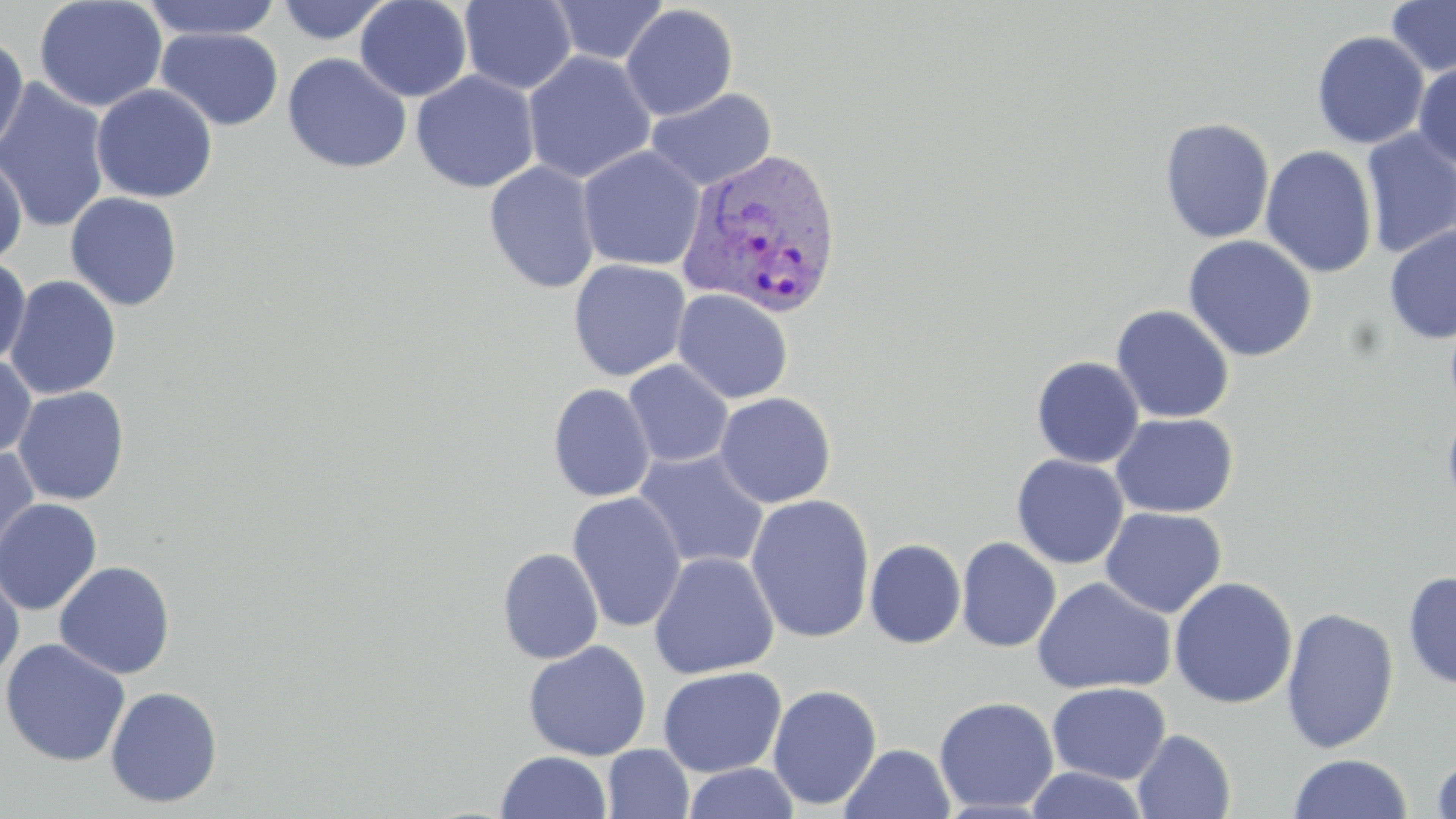

{
  "slide_level_diagnosis": "Plasmodium vivax",
  "magnification": "1000x",
  "uninfected_red_blood_cell_locations": "approximate bounding boxes as named x1/y1/x2/y2 corners in pixels: (x1=33, y1=0, x2=168, y2=113), (x1=138, y1=0, x2=285, y2=41), (x1=354, y1=0, x2=473, y2=102), (x1=1386, y1=0, x2=1456, y2=78), (x1=275, y1=1, x2=395, y2=44), (x1=458, y1=1, x2=577, y2=94), (x1=548, y1=1, x2=669, y2=65), (x1=620, y1=4, x2=739, y2=121), (x1=155, y1=27, x2=284, y2=131), (x1=1311, y1=30, x2=1429, y2=150), (x1=0, y1=34, x2=29, y2=159), (x1=522, y1=50, x2=657, y2=184), (x1=282, y1=52, x2=412, y2=174), (x1=1413, y1=62, x2=1456, y2=169), (x1=410, y1=70, x2=540, y2=193), (x1=0, y1=78, x2=111, y2=234), (x1=91, y1=83, x2=218, y2=203), (x1=644, y1=87, x2=777, y2=191), (x1=1158, y1=117, x2=1275, y2=244), (x1=1361, y1=128, x2=1456, y2=260), (x1=1260, y1=145, x2=1378, y2=278), (x1=577, y1=146, x2=704, y2=271), (x1=0, y1=151, x2=27, y2=269), (x1=483, y1=160, x2=601, y2=295), (x1=65, y1=191, x2=184, y2=311), (x1=1384, y1=225, x2=1456, y2=344), (x1=1182, y1=235, x2=1318, y2=362), (x1=0, y1=257, x2=31, y2=367), (x1=568, y1=259, x2=691, y2=381), (x1=4, y1=275, x2=121, y2=400), (x1=673, y1=288, x2=794, y2=404), (x1=1444, y1=302, x2=1456, y2=420), (x1=1110, y1=305, x2=1235, y2=424), (x1=0, y1=355, x2=37, y2=461), (x1=1030, y1=356, x2=1145, y2=468), (x1=622, y1=360, x2=734, y2=468), (x1=547, y1=383, x2=656, y2=503), (x1=12, y1=386, x2=130, y2=506), (x1=715, y1=391, x2=837, y2=508), (x1=1442, y1=403, x2=1456, y2=518), (x1=1110, y1=412, x2=1238, y2=518), (x1=0, y1=446, x2=40, y2=573), (x1=633, y1=448, x2=770, y2=571), (x1=1011, y1=454, x2=1129, y2=569), (x1=567, y1=491, x2=687, y2=633), (x1=745, y1=494, x2=876, y2=644), (x1=0, y1=497, x2=103, y2=615), (x1=1100, y1=506, x2=1227, y2=619), (x1=956, y1=537, x2=1061, y2=652), (x1=864, y1=538, x2=967, y2=649), (x1=497, y1=547, x2=604, y2=665), (x1=648, y1=551, x2=780, y2=679), (x1=54, y1=561, x2=176, y2=680), (x1=0, y1=564, x2=25, y2=680), (x1=1402, y1=570, x2=1456, y2=690), (x1=1167, y1=576, x2=1298, y2=709), (x1=1032, y1=577, x2=1177, y2=695), (x1=1280, y1=606, x2=1399, y2=753), (x1=0, y1=638, x2=131, y2=766), (x1=523, y1=641, x2=651, y2=761), (x1=657, y1=666, x2=788, y2=777), (x1=1047, y1=682, x2=1171, y2=784), (x1=767, y1=683, x2=882, y2=811), (x1=105, y1=685, x2=223, y2=808), (x1=934, y1=696, x2=1059, y2=814), (x1=1133, y1=729, x2=1236, y2=819), (x1=839, y1=743, x2=955, y2=819), (x1=603, y1=745, x2=694, y2=819), (x1=495, y1=750, x2=612, y2=819), (x1=1430, y1=751, x2=1456, y2=818), (x1=1288, y1=753, x2=1414, y2=818), (x1=682, y1=762, x2=801, y2=819), (x1=1024, y1=767, x2=1149, y2=819)",
  "image_size": "1456×819 pixels",
  "stain": "May-Grünwald-Giemsa",
  "plasmodium_vivax_infected_red_blood_cell_locations": "approximate bounding boxes as named x1/y1/x2/y2 corners in pixels: (x1=677, y1=146, x2=844, y2=319)",
  "preparation": "thin blood smear",
  "field_of_view": "one of a larger specimen",
  "modality": "light microscopy"
}